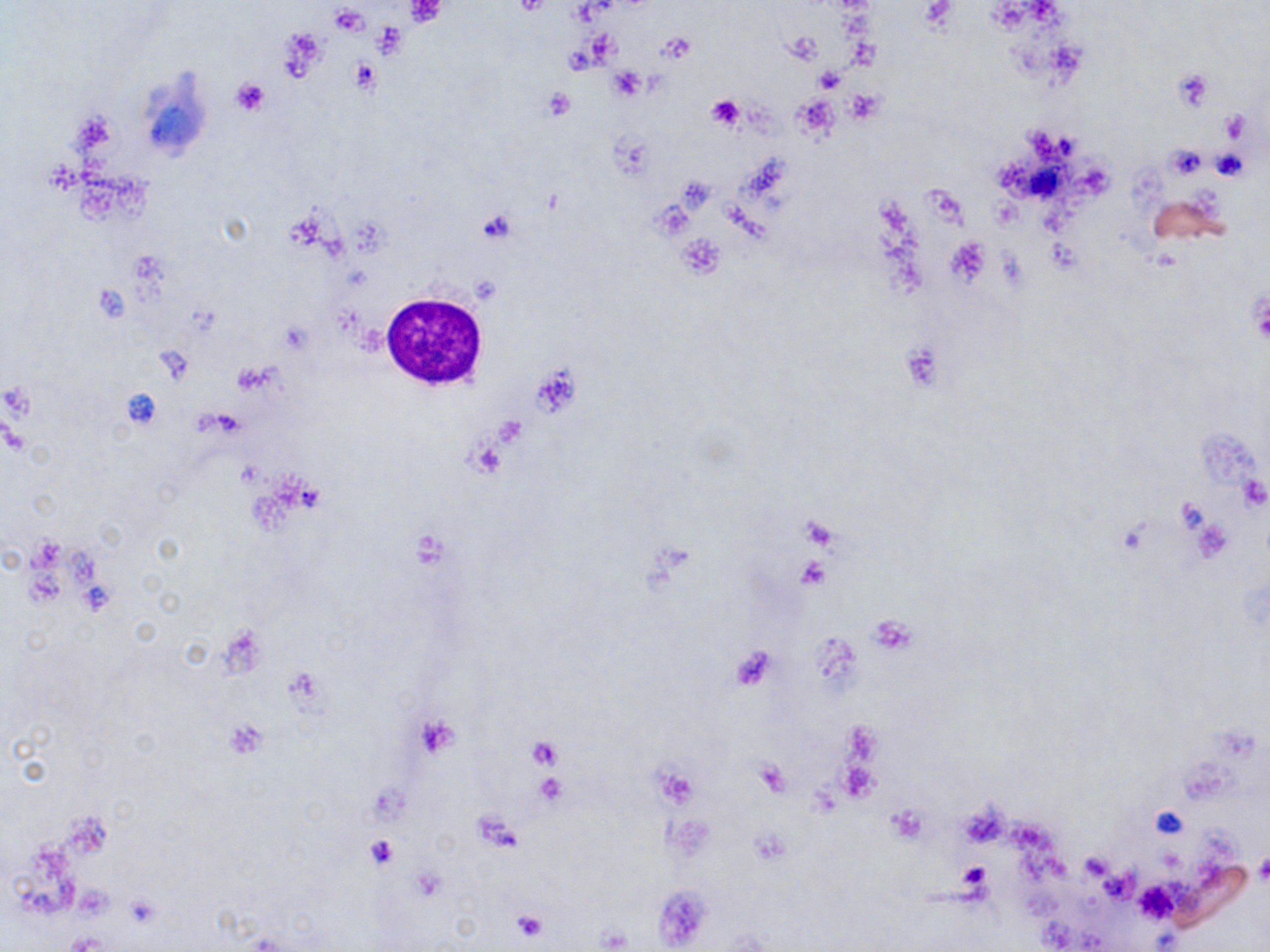
Summary:
  - Coordinate format: approximate bounding boxes as (x1,y1)-(x2,y2) corner pairs in pixels
  - White blood cell locations: (380,291)-(489,392)
  - Platelet locations: (405,1)-(447,26), (512,1)-(552,18), (329,4)-(368,34), (782,33)-(819,65), (658,35)-(696,65), (350,58)-(380,95), (1172,67)-(1214,112), (815,70)-(844,94), (230,76)-(271,116), (541,88)-(574,122), (844,88)-(885,123), (791,93)-(839,140), (706,95)-(745,131), (1221,109)-(1250,143), (1210,145)-(1252,182), (1164,146)-(1207,181), (476,208)-(518,246), (676,234)-(723,277), (946,235)-(992,287), (1249,296)-(1270,346), (528,363)-(582,418), (468,439)-(505,477), (798,557)-(830,591), (868,617)-(916,655), (809,629)-(864,700), (223,717)-(268,758), (526,737)-(562,770), (754,758)-(790,797), (839,761)-(882,805), (653,764)-(700,807), (534,773)-(569,805), (955,800)-(1007,848), (887,806)-(927,843), (1150,806)-(1187,841), (475,814)-(523,852), (364,835)-(401,870), (1079,852)-(1116,882), (1254,853)-(1270,887), (958,862)-(990,893), (122,892)-(162,928), (510,907)-(548,943), (597,925)-(631,950)
  - Slide-level diagnosis: negative for blood parasites
  - Magnification: 1000x
  - Modality: light microscopy
  - Stain: May-Grünwald-Giemsa
  - Field of view: one of a larger specimen
  - Image size: 1270×952 pixels
  - Preparation: thin blood smear